Report the malaria status of this cell.
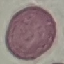
It is uninfected.

Summary:
  - Image type: cell patch, automatically extracted from a larger field of view and resized to 64 × 64 pixels
  - Stain: Giemsa
  - Capture: smartphone camera at the microscope eyepiece
  - Preparation: thin blood smear